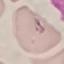

result = malaria parasites identified
capture = smartphone through the microscope eyepiece
image type = cell patch, automatically extracted from a larger field of view and resized to 64 × 64 pixels
preparation = thin smear
stain = Giemsa